Draw a bounding box around every leukocyte (white blood cell).
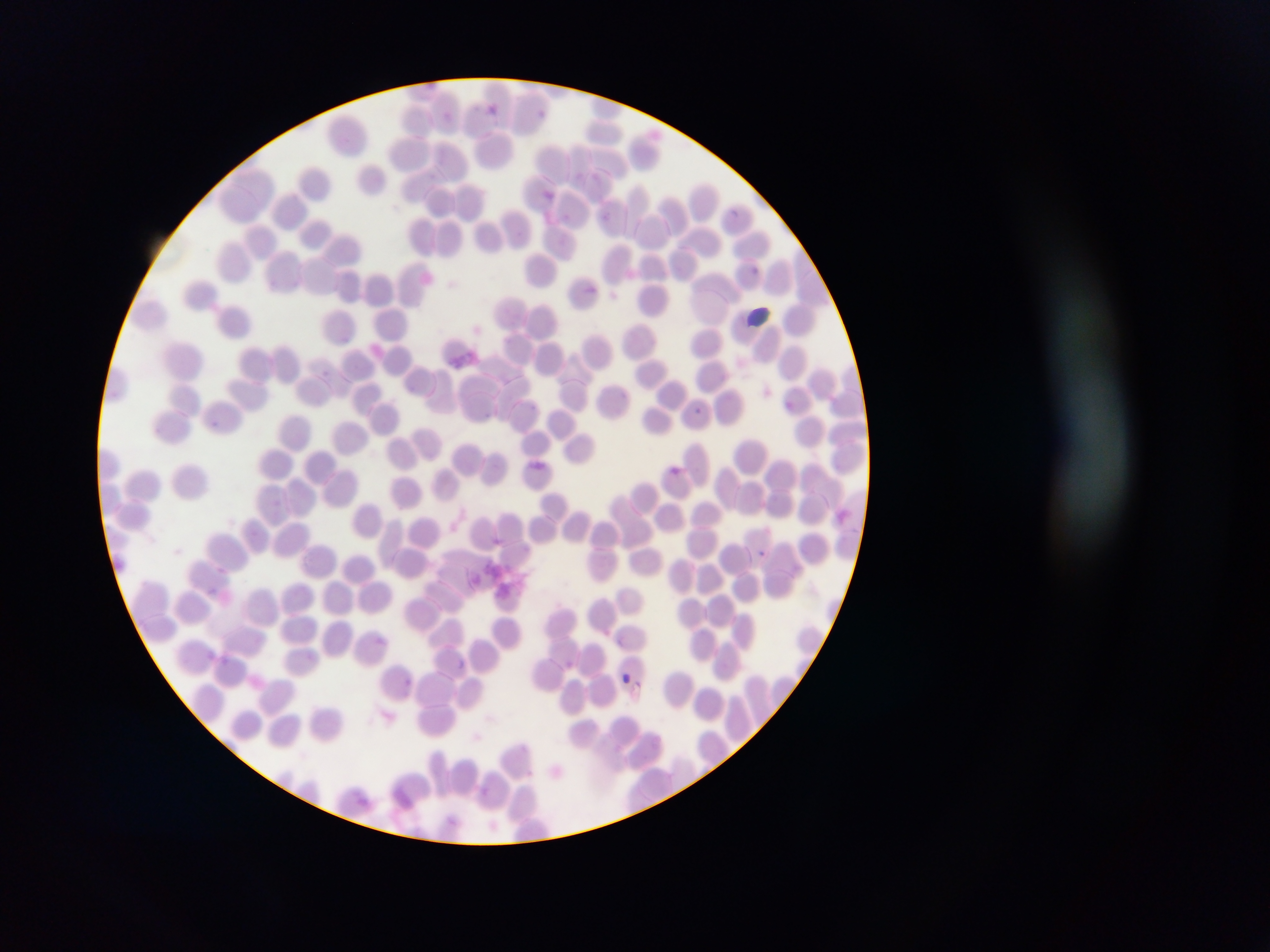

No leukocytes observed.

Approximate bounding boxes as left top right bottom in pixels.
Summary:
  - Malaria parasite locations: 488 101 509 127; 535 105 552 121; 444 108 456 117; 543 187 555 199; 729 206 740 220; 535 208 557 234; 749 265 768 286; 580 281 602 300; 783 397 795 414; 693 406 706 421; 670 466 679 474; 759 548 771 563; 209 584 230 605; 374 633 386 647; 204 651 217 661; 220 651 231 668; 456 656 468 669; 400 666 417 704; 617 670 633 687
  - Country: Ghana
  - Image size: 1270×952 pixels
  - Field of view: single
  - Capture: mobile-phone photograph through a microscope
  - Preparation: thin blood smear